Outline platelets.
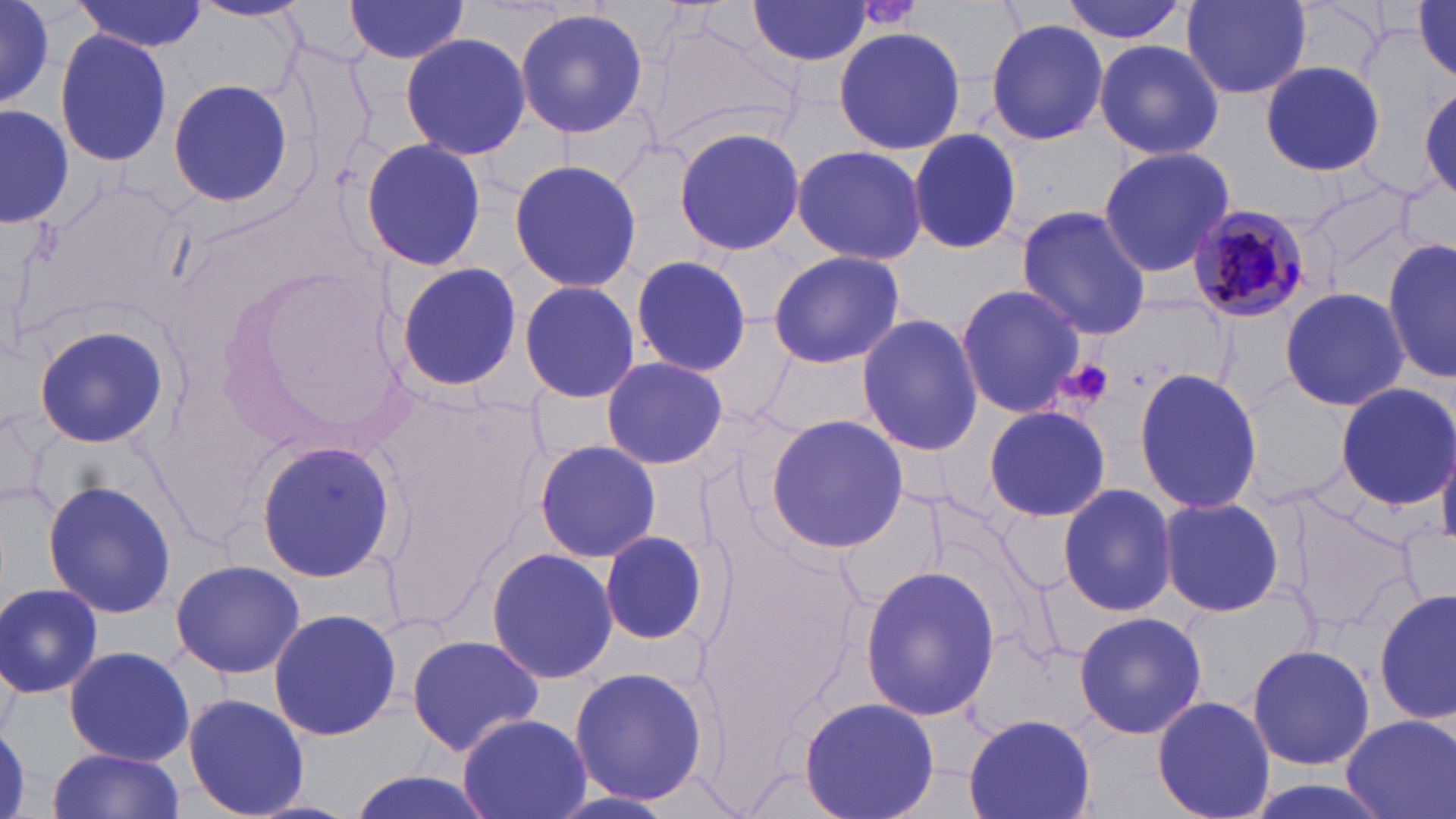
Approximate bounding boxes as named x1/y1/x2/y2 corners in pixels.
Platelets: (x1=1055, y1=358, x2=1117, y2=412).

Summary:
  - Plasmodium malariae-infected red blood cell locations: (x1=1185, y1=204, x2=1312, y2=324)
  - Uninfected red blood cell locations: (x1=73, y1=0, x2=207, y2=53), (x1=1057, y1=0, x2=1189, y2=45), (x1=188, y1=1, x2=309, y2=22), (x1=1180, y1=1, x2=1312, y2=100), (x1=1411, y1=1, x2=1456, y2=82), (x1=343, y1=2, x2=476, y2=64), (x1=748, y1=2, x2=875, y2=67), (x1=0, y1=5, x2=58, y2=104), (x1=514, y1=6, x2=650, y2=138), (x1=639, y1=15, x2=801, y2=159), (x1=986, y1=18, x2=1107, y2=147), (x1=832, y1=23, x2=966, y2=159), (x1=53, y1=29, x2=174, y2=169), (x1=399, y1=32, x2=530, y2=160), (x1=1092, y1=38, x2=1224, y2=162), (x1=1260, y1=61, x2=1385, y2=176), (x1=167, y1=78, x2=294, y2=208), (x1=0, y1=102, x2=73, y2=231), (x1=672, y1=125, x2=807, y2=256), (x1=907, y1=129, x2=1025, y2=254), (x1=358, y1=136, x2=487, y2=270), (x1=789, y1=145, x2=929, y2=266), (x1=1096, y1=146, x2=1237, y2=279), (x1=507, y1=159, x2=642, y2=291), (x1=1300, y1=175, x2=1427, y2=276), (x1=1015, y1=206, x2=1151, y2=340), (x1=1383, y1=235, x2=1456, y2=386), (x1=766, y1=249, x2=907, y2=369), (x1=630, y1=253, x2=752, y2=377), (x1=393, y1=261, x2=522, y2=395), (x1=518, y1=279, x2=640, y2=405), (x1=955, y1=282, x2=1087, y2=419), (x1=1280, y1=285, x2=1409, y2=411), (x1=856, y1=314, x2=984, y2=455), (x1=33, y1=321, x2=167, y2=451), (x1=599, y1=356, x2=729, y2=470), (x1=1133, y1=371, x2=1264, y2=514), (x1=1334, y1=381, x2=1455, y2=509), (x1=983, y1=404, x2=1110, y2=523), (x1=0, y1=406, x2=52, y2=514), (x1=766, y1=412, x2=909, y2=554), (x1=253, y1=440, x2=398, y2=584), (x1=533, y1=440, x2=662, y2=563), (x1=41, y1=479, x2=177, y2=619), (x1=1058, y1=483, x2=1177, y2=616), (x1=1281, y1=489, x2=1421, y2=635), (x1=1159, y1=496, x2=1285, y2=616), (x1=595, y1=529, x2=710, y2=647), (x1=485, y1=549, x2=620, y2=685), (x1=169, y1=558, x2=307, y2=681), (x1=860, y1=565, x2=999, y2=722), (x1=0, y1=582, x2=104, y2=699), (x1=1376, y1=588, x2=1456, y2=723), (x1=267, y1=608, x2=402, y2=741), (x1=1073, y1=611, x2=1207, y2=739), (x1=406, y1=634, x2=545, y2=756), (x1=1246, y1=643, x2=1375, y2=770), (x1=64, y1=645, x2=194, y2=767), (x1=569, y1=666, x2=710, y2=804), (x1=183, y1=693, x2=312, y2=818), (x1=800, y1=696, x2=940, y2=819), (x1=1152, y1=696, x2=1277, y2=819), (x1=962, y1=711, x2=1095, y2=819), (x1=457, y1=712, x2=591, y2=819), (x1=1342, y1=713, x2=1456, y2=819), (x1=46, y1=749, x2=185, y2=819), (x1=340, y1=771, x2=499, y2=819)
  - Slide-level diagnosis: Plasmodium malariae
  - Preparation: thin blood film
  - Stain: May-Grünwald-Giemsa
  - Image size: 1456×819 pixels
  - Field of view: one of a larger specimen
  - Modality: light microscopy
  - Magnification: 1000x